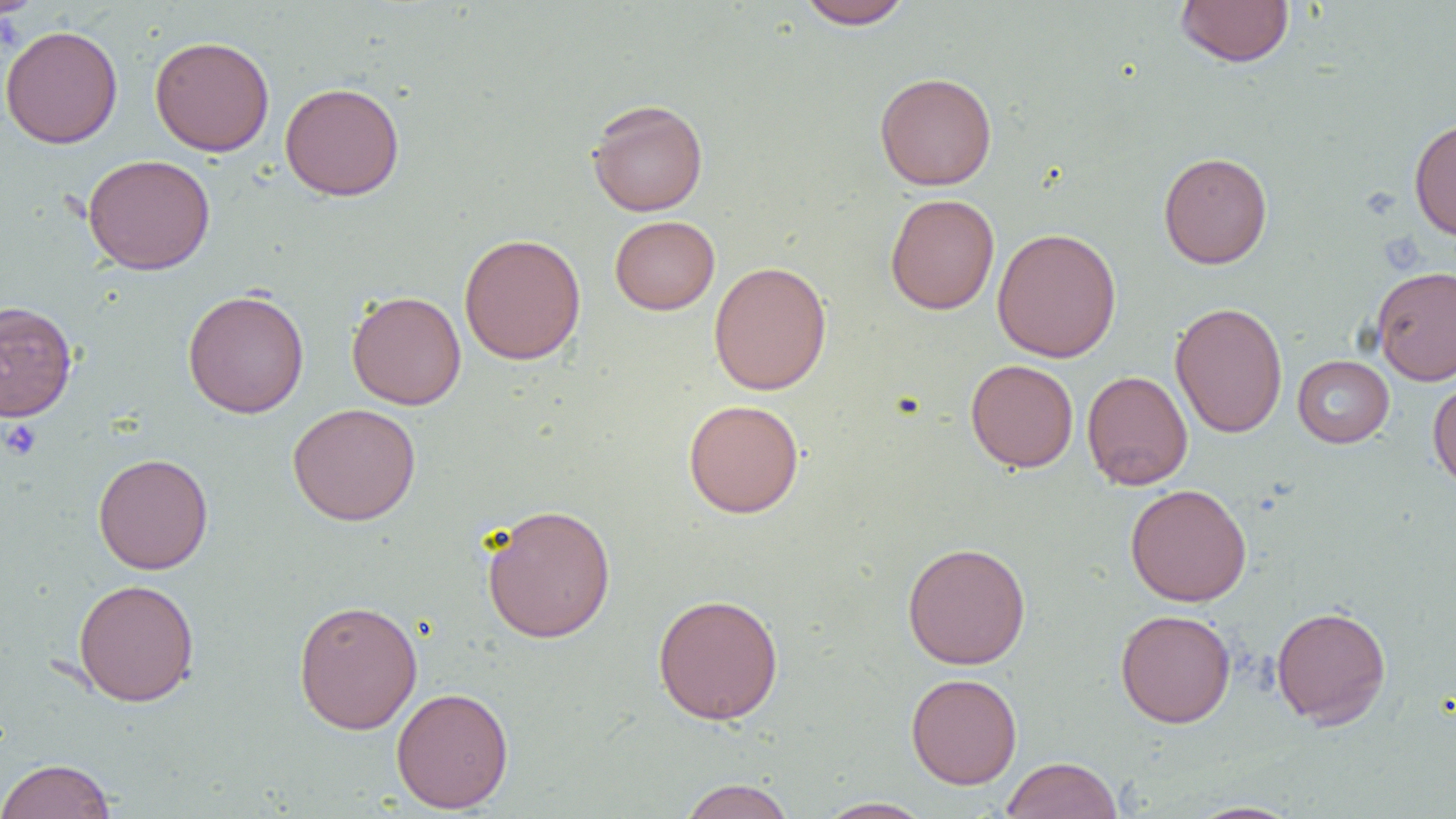

{
  "slide_level_diagnosis": "negative for blood parasites",
  "image_size": "1456×819 pixels",
  "uninfected_red_blood_cell_locations": "approximate bounding boxes as (x1, y1, x2, y2) in pixels: (1, 0, 47, 19), (796, 0, 913, 30), (1175, 0, 1294, 67), (0, 24, 124, 148), (149, 35, 275, 157), (874, 72, 998, 190), (279, 82, 405, 201), (586, 98, 709, 216), (1409, 116, 1456, 241), (1158, 151, 1273, 269), (82, 154, 216, 275), (885, 193, 999, 315), (609, 215, 720, 315), (992, 227, 1122, 362), (459, 232, 586, 365), (708, 260, 832, 396), (1371, 265, 1456, 385), (182, 289, 309, 418), (347, 290, 466, 410), (0, 300, 78, 422), (1170, 301, 1287, 439), (1292, 355, 1394, 447), (965, 359, 1079, 472), (1081, 370, 1193, 490), (1427, 377, 1456, 492), (683, 399, 804, 518), (287, 403, 421, 525), (93, 452, 214, 575), (1125, 483, 1252, 607), (481, 504, 617, 643), (902, 541, 1031, 670), (73, 578, 200, 706), (652, 593, 784, 725), (293, 599, 423, 734), (1271, 605, 1391, 728), (1115, 609, 1236, 727), (906, 672, 1022, 789), (391, 687, 514, 813), (1001, 756, 1123, 818), (0, 758, 117, 819), (678, 778, 796, 819), (815, 797, 935, 818), (1183, 801, 1305, 819)",
  "magnification": "1000x",
  "field_of_view": "single",
  "preparation": "thin blood film",
  "modality": "optical microscopy",
  "platelet_locations": "approximate bounding boxes as (x1, y1, x2, y2) in pixels: (1, 419, 42, 461)"
}